Comment on the morphology of the red blood cells.
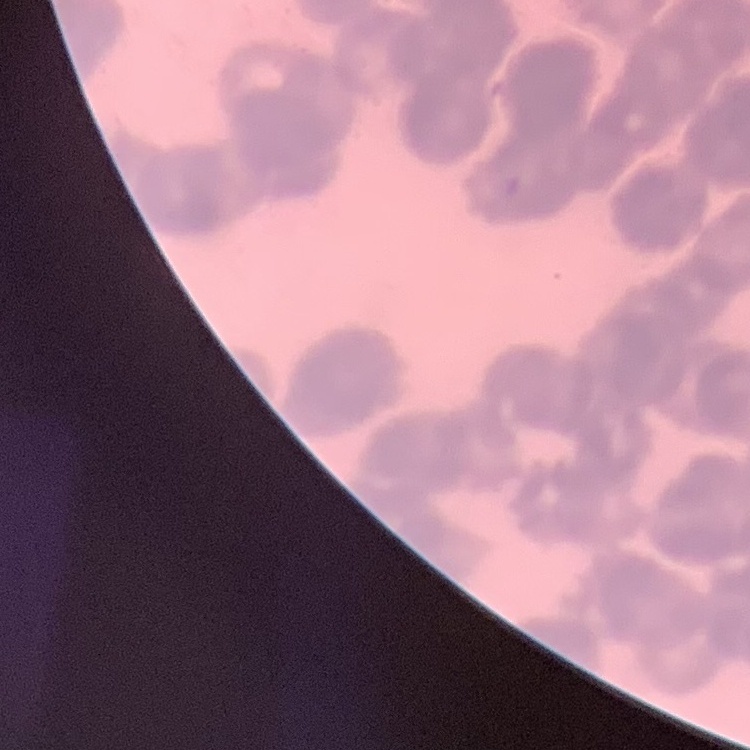
They show rouleaux formation.

stain = Field's or Giemsa
image type = square crop of a larger photomicrograph
preparation = thin peripheral smear